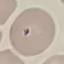

Summary:
  - Malaria status: uninfected
  - Capture: smartphone camera at the microscope eyepiece
  - Stain: Giemsa
  - Image type: automatically extracted cell patch, resized to 64 × 64 pixels
  - Preparation: thin blood smear